Assess for Plasmodium parasites.
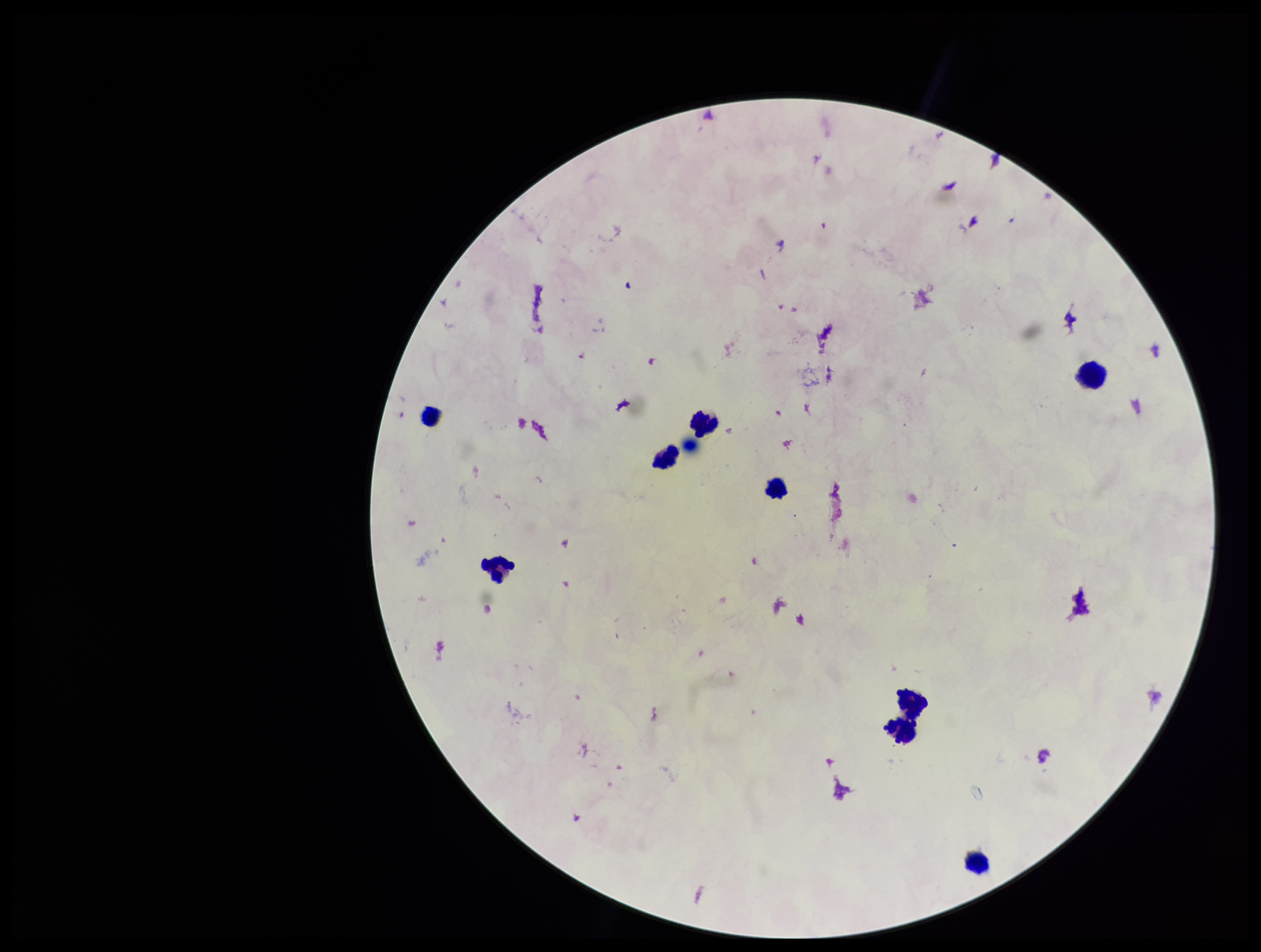
None seen.

Stained with Giemsa. Parasite count: 0. Patient malaria status: negative. Preparation: thick smear. Photographed through the microscope eyepiece with a smartphone camera. Leukocyte count: 8. Image is 1261×952 pixels. One field from this slide.